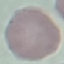 Malaria status: uninfected. Thin smear of blood. Photographed with a smartphone camera at the microscope eyepiece. Cell patch, automatically extracted from a larger field of view and resized to 64 × 64 pixels. Giemsa-stained preparation.